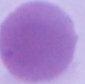
magnification = 1000x
modality = photomicrograph
identification = red blood cell